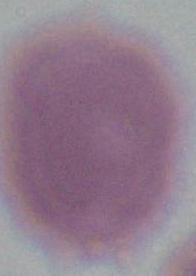

identification = red blood cell
magnification = 1000x
modality = micrograph